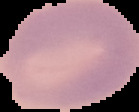 Cell region segmented out of the field of view; the surrounding area is masked to black. Result: negative for Plasmodium parasites. From a thin blood smear. Image is 139×112 pixels.